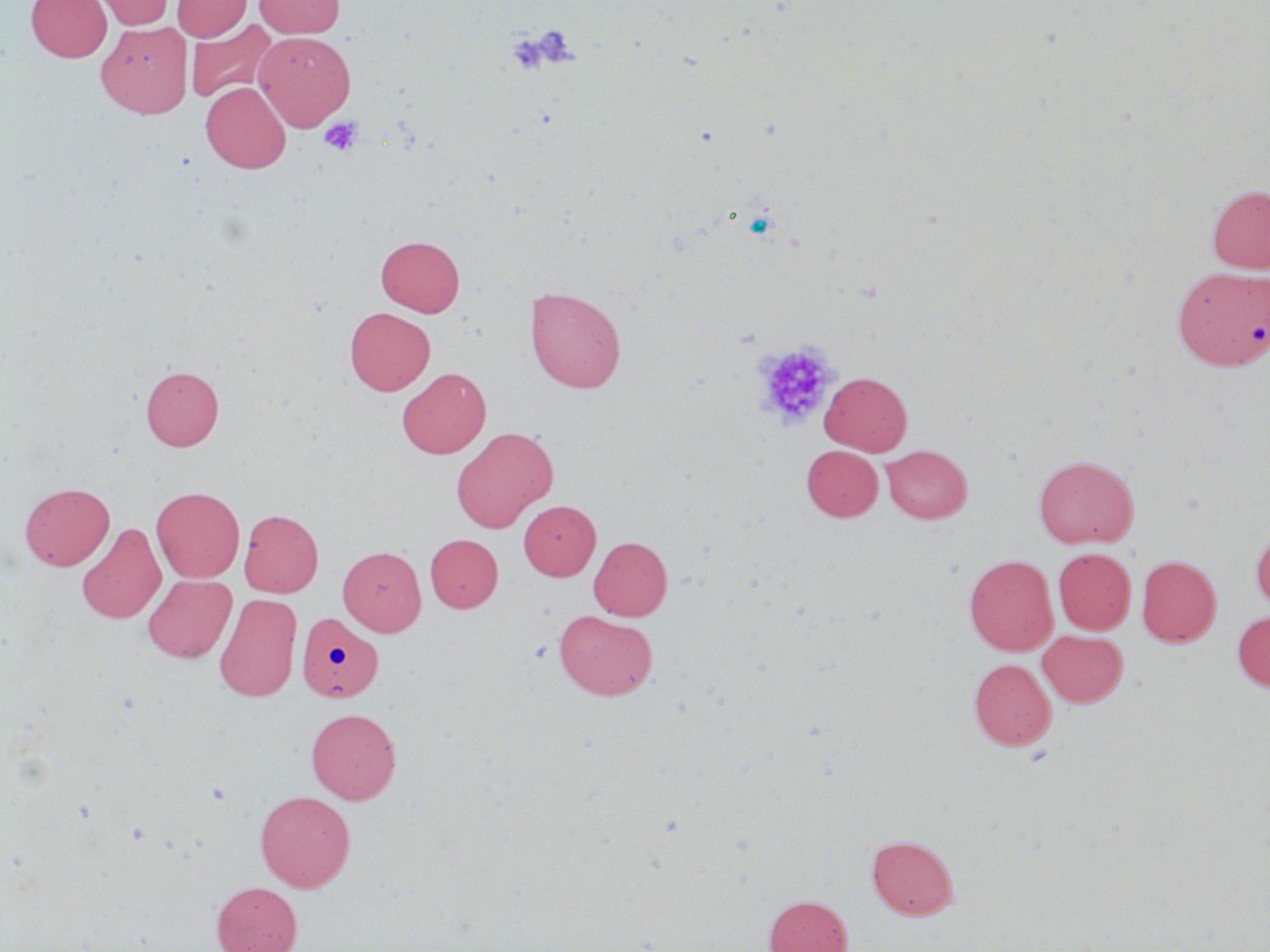
slide-level diagnosis = negative for blood parasites
image size = 1270×952 pixels
field of view = single
uninfected red blood cell locations = approximate bounding boxes as [x1, y1, x2, y2] in pixels: [27, 0, 111, 62], [91, 0, 174, 29], [172, 0, 250, 41], [254, 0, 344, 38], [186, 19, 276, 103], [97, 21, 192, 119], [254, 31, 355, 131], [201, 82, 291, 173], [1208, 185, 1270, 273], [376, 235, 465, 316], [1172, 264, 1268, 368], [525, 286, 626, 393], [344, 307, 435, 395], [141, 365, 224, 451], [397, 368, 490, 458], [820, 372, 912, 455], [451, 426, 557, 532], [801, 445, 883, 521], [881, 445, 973, 523], [1033, 455, 1139, 548], [19, 483, 114, 570], [152, 486, 245, 582], [519, 500, 600, 580], [239, 509, 323, 597], [76, 522, 166, 624], [1251, 528, 1270, 615], [425, 534, 502, 612], [589, 536, 673, 621], [338, 546, 426, 636], [1053, 548, 1135, 634], [964, 555, 1058, 655], [1136, 555, 1221, 646], [142, 574, 237, 663], [214, 593, 302, 702], [554, 609, 658, 700], [1233, 611, 1270, 691], [297, 612, 383, 702], [1038, 630, 1128, 707], [969, 658, 1056, 750], [306, 708, 401, 804], [255, 790, 355, 892], [867, 834, 959, 920], [212, 881, 301, 952], [764, 894, 852, 952]
modality = optical microscopy
preparation = thin blood smear
magnification = 1000x
platelet locations = approximate bounding boxes as [x1, y1, x2, y2] in pixels: [517, 24, 580, 71], [506, 31, 557, 76], [320, 116, 364, 156], [753, 341, 838, 429]
stain = May-Grünwald-Giemsa